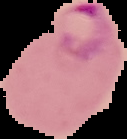

Summary:
  - Malaria status: parasitized
  - Image type: cell region segmented out of the field of view; surrounding area masked to black
  - Preparation: thin blood film
  - Image size: 127×139 pixels